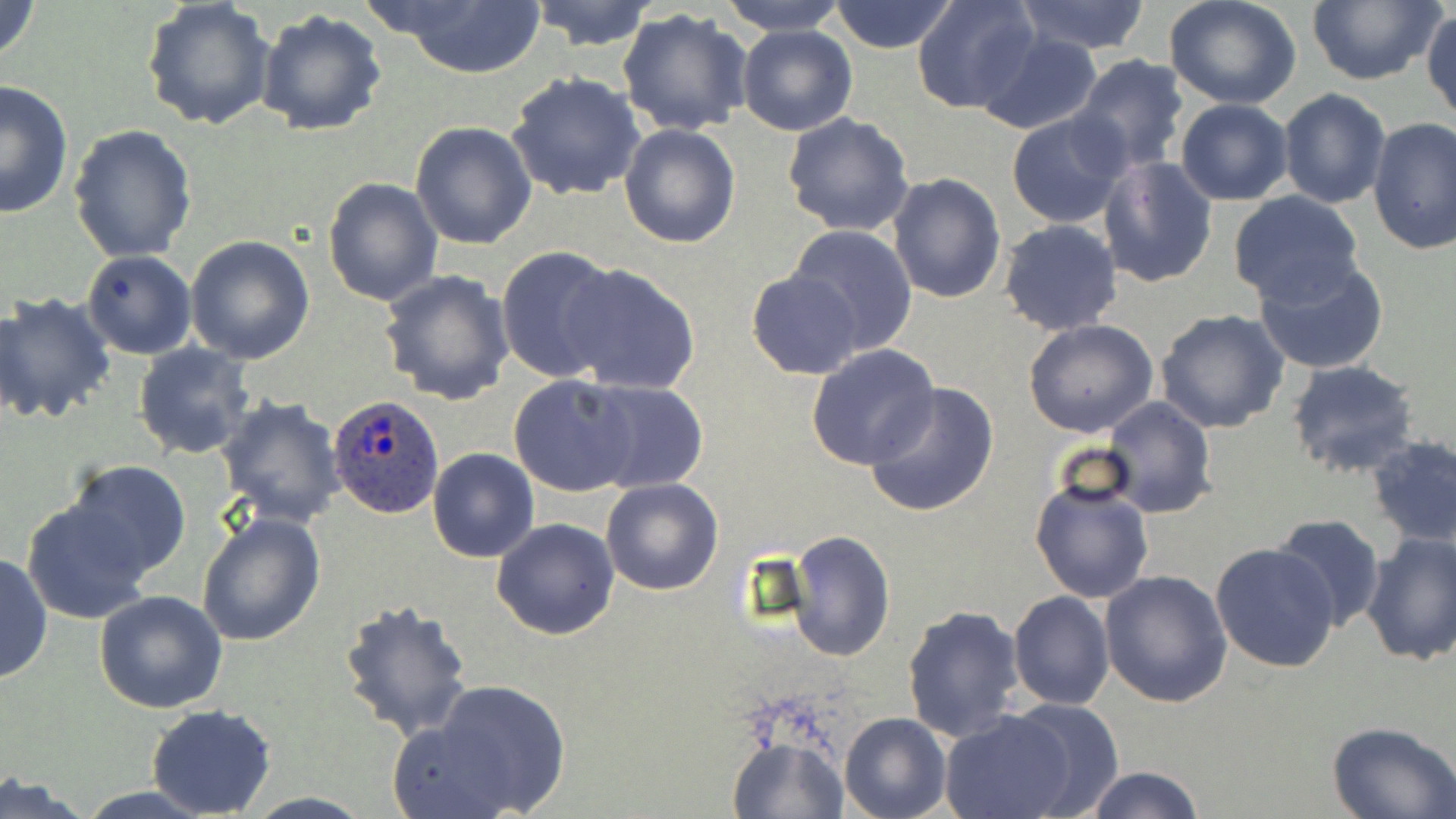
Summary:
  - Coordinate format: approximate bounding boxes as named x1/y1/x2/y2 corners in pixels
  - Plasmodium ovale-infected red blood cell locations: (x1=327, y1=396, x2=444, y2=519)
  - Uninfected red blood cell locations: (x1=0, y1=0, x2=43, y2=69), (x1=526, y1=0, x2=658, y2=51), (x1=718, y1=0, x2=850, y2=36), (x1=827, y1=0, x2=960, y2=54), (x1=911, y1=0, x2=1041, y2=116), (x1=1013, y1=0, x2=1153, y2=54), (x1=1304, y1=0, x2=1442, y2=86), (x1=141, y1=1, x2=277, y2=134), (x1=386, y1=1, x2=547, y2=77), (x1=1164, y1=1, x2=1303, y2=110), (x1=617, y1=7, x2=755, y2=138), (x1=1422, y1=7, x2=1455, y2=126), (x1=255, y1=9, x2=387, y2=138), (x1=736, y1=23, x2=857, y2=136), (x1=974, y1=31, x2=1104, y2=134), (x1=1072, y1=55, x2=1190, y2=174), (x1=506, y1=72, x2=645, y2=202), (x1=0, y1=79, x2=76, y2=219), (x1=1278, y1=87, x2=1391, y2=208), (x1=1174, y1=98, x2=1293, y2=205), (x1=1006, y1=109, x2=1130, y2=228), (x1=782, y1=113, x2=915, y2=238), (x1=1367, y1=117, x2=1456, y2=255), (x1=409, y1=121, x2=538, y2=250), (x1=618, y1=124, x2=741, y2=248), (x1=69, y1=126, x2=199, y2=263), (x1=1098, y1=156, x2=1219, y2=288), (x1=886, y1=170, x2=1006, y2=304), (x1=322, y1=176, x2=443, y2=308), (x1=1227, y1=190, x2=1363, y2=306), (x1=998, y1=219, x2=1123, y2=336), (x1=787, y1=224, x2=917, y2=356), (x1=185, y1=235, x2=315, y2=364), (x1=496, y1=244, x2=621, y2=383), (x1=81, y1=250, x2=197, y2=358), (x1=1254, y1=256, x2=1389, y2=376), (x1=559, y1=262, x2=702, y2=395), (x1=378, y1=269, x2=515, y2=407), (x1=748, y1=271, x2=862, y2=379), (x1=0, y1=291, x2=118, y2=426), (x1=1154, y1=308, x2=1290, y2=433), (x1=1023, y1=318, x2=1159, y2=439), (x1=132, y1=342, x2=255, y2=460), (x1=805, y1=343, x2=939, y2=470), (x1=1285, y1=360, x2=1421, y2=479), (x1=509, y1=374, x2=637, y2=497), (x1=582, y1=378, x2=708, y2=492), (x1=865, y1=381, x2=1000, y2=519), (x1=215, y1=396, x2=346, y2=527), (x1=1102, y1=396, x2=1216, y2=518), (x1=1365, y1=433, x2=1456, y2=547), (x1=428, y1=449, x2=539, y2=562), (x1=64, y1=459, x2=193, y2=582), (x1=1031, y1=476, x2=1154, y2=604), (x1=601, y1=478, x2=723, y2=595), (x1=23, y1=498, x2=157, y2=624), (x1=196, y1=511, x2=327, y2=649), (x1=1271, y1=513, x2=1385, y2=631), (x1=491, y1=518, x2=620, y2=639), (x1=785, y1=530, x2=896, y2=662), (x1=1361, y1=533, x2=1456, y2=666), (x1=1210, y1=543, x2=1340, y2=673), (x1=0, y1=552, x2=51, y2=685), (x1=1099, y1=569, x2=1233, y2=707), (x1=95, y1=591, x2=228, y2=714), (x1=1007, y1=592, x2=1114, y2=710), (x1=338, y1=598, x2=475, y2=742), (x1=901, y1=604, x2=1027, y2=744), (x1=398, y1=679, x2=571, y2=819), (x1=145, y1=704, x2=278, y2=818), (x1=939, y1=710, x2=1079, y2=819), (x1=840, y1=712, x2=952, y2=819), (x1=1328, y1=720, x2=1456, y2=818), (x1=728, y1=735, x2=847, y2=818), (x1=1079, y1=765, x2=1205, y2=819), (x1=0, y1=776, x2=97, y2=818)
  - Slide-level diagnosis: Plasmodium ovale
  - Modality: light microscopy
  - Image size: 1456×819 pixels
  - Stain: May-Grünwald-Giemsa
  - Field of view: one of a larger specimen
  - Magnification: 1000x
  - Preparation: thin blood smear